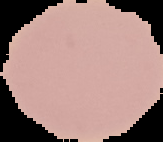

From a thin blood film. Image is 163×142 pixels. Malaria status: uninfected. Segmented cell region on a black background.